Name the blood parasite species.
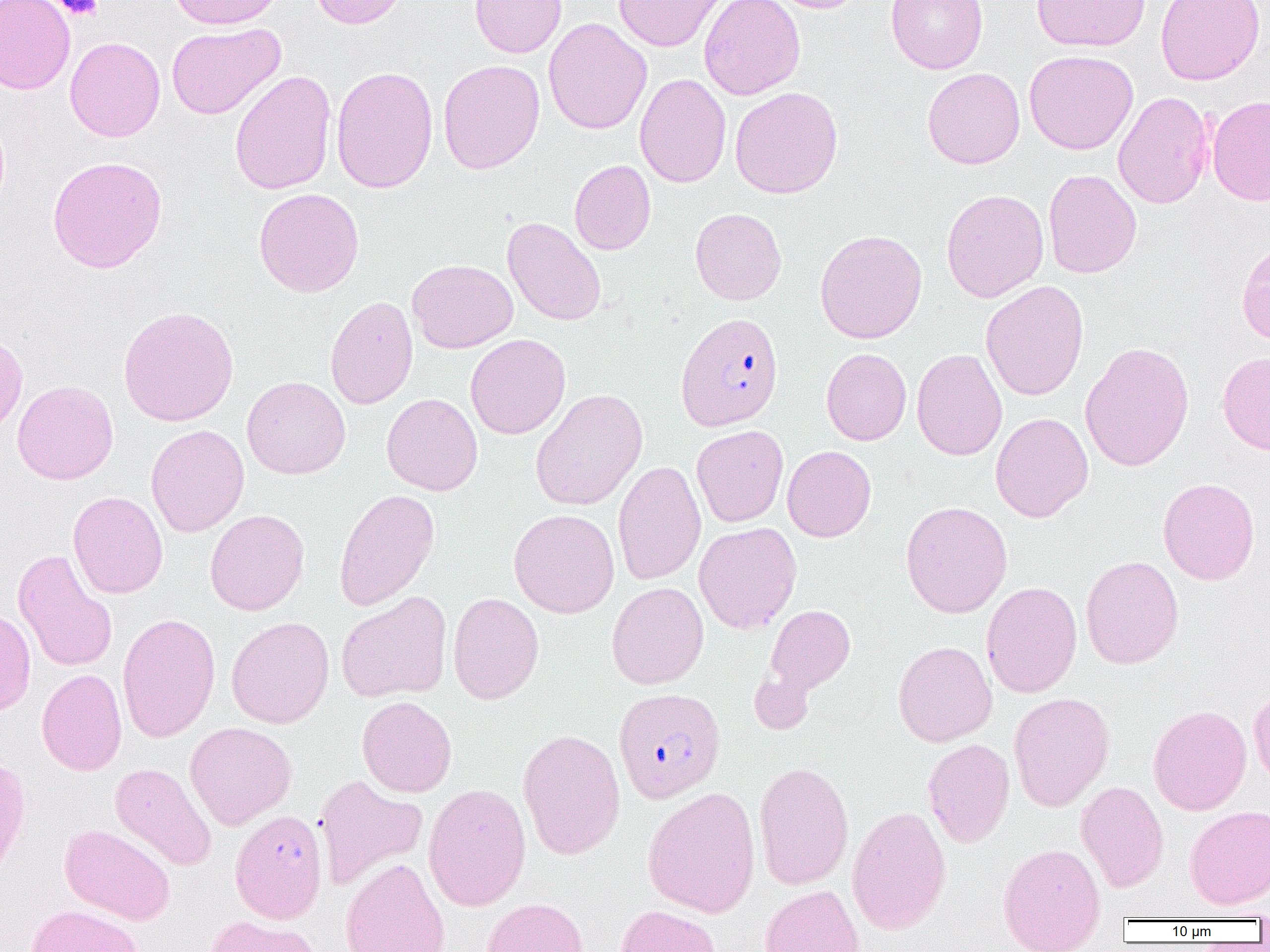

Plasmodium falciparum.

Summary:
  - Coordinate format: approximate bounding boxes as (x1,y1)-(x2,y2) corner pairs in pixels
  - Plasmodium falciparum-infected red blood cell locations: (675,312)-(784,431), (619,687)-(732,803), (229,809)-(328,923)
  - Platelet locations: (54,0)-(103,20)
  - Uninfected red blood cell locations: (0,0)-(75,94), (167,0)-(285,29), (309,0)-(411,29), (469,0)-(567,58), (613,0)-(726,52), (698,0)-(805,100), (765,0)-(870,13), (886,0)-(988,74), (1032,0)-(1151,52), (1155,1)-(1266,85), (543,17)-(652,135), (166,23)-(285,120), (65,37)-(165,142), (1024,49)-(1138,155), (438,59)-(545,174), (331,65)-(438,194), (923,67)-(1025,169), (229,70)-(337,195), (635,73)-(731,188), (730,86)-(843,199), (1112,91)-(1214,210), (1207,95)-(1270,206), (47,155)-(168,274), (569,160)-(656,255), (1042,168)-(1142,278), (254,188)-(364,297), (940,188)-(1049,302), (690,208)-(787,305), (502,216)-(606,326), (814,229)-(927,344), (407,259)-(518,353), (980,280)-(1089,401), (325,295)-(418,410), (118,305)-(239,427), (0,332)-(28,438), (465,334)-(570,440), (1080,341)-(1195,472), (821,348)-(912,445), (911,348)-(1008,461), (1217,351)-(1270,455), (242,376)-(351,479), (12,380)-(119,484), (530,388)-(648,511), (381,393)-(483,496), (990,412)-(1093,523), (146,424)-(249,537), (691,424)-(789,527), (782,445)-(876,542), (613,459)-(706,586), (1158,477)-(1260,585), (334,489)-(440,611), (68,491)-(168,599), (900,501)-(1012,618), (508,508)-(620,618), (205,509)-(309,615), (694,522)-(802,634), (12,548)-(118,673), (1081,555)-(1184,669), (606,581)-(709,689), (980,581)-(1082,698), (336,591)-(452,703), (448,592)-(544,704), (764,604)-(855,694), (0,606)-(36,717), (117,612)-(220,743), (226,616)-(334,728), (893,640)-(996,747), (749,667)-(816,735), (36,668)-(127,776), (1249,685)-(1270,788), (1008,692)-(1114,811), (357,696)-(457,797), (1148,704)-(1252,816), (184,722)-(297,830), (518,728)-(626,859), (923,738)-(1015,848), (0,754)-(31,878), (753,760)-(854,891), (109,762)-(217,871), (314,773)-(428,891), (1075,780)-(1169,893), (423,783)-(532,910), (642,786)-(761,918), (846,805)-(951,934), (1184,805)-(1270,910), (59,823)-(176,925), (997,842)-(1106,952), (339,856)-(450,952), (760,885)-(865,952), (482,898)-(588,952), (25,904)-(143,952), (615,904)-(721,952), (204,915)-(322,952)
  - Field of view: one of a larger specimen
  - Preparation: thin blood smear
  - Image size: 1270×952 pixels
  - Magnification: 1000x
  - Modality: light microscopy